Outline each blood parasite and name the species.
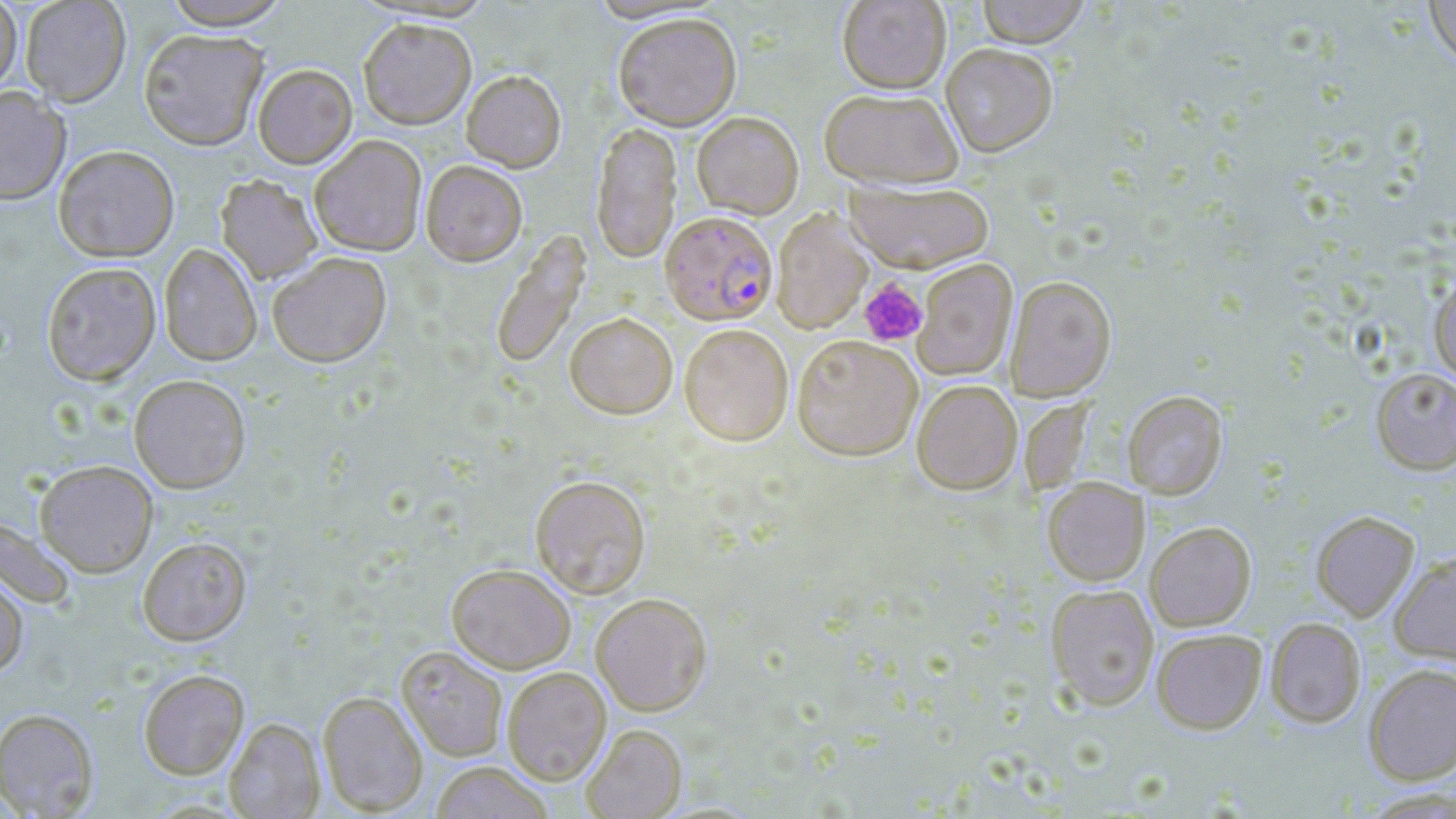
Approximate bounding boxes as (x1,y1)-(x2,y2) corner pairs in pixels.
Plasmodium falciparum-infected red blood cells: (660,211)-(777,325).
No Plasmodium ovale, Plasmodium malariae, Plasmodium vivax, Babesia divergens, or Trypanosoma brucei observed.

Uninfected red blood cell locations: (0,0)-(22,95), (20,0)-(131,106), (160,0)-(292,30), (837,0)-(951,93), (975,0)-(1092,47), (1424,0)-(1456,71), (612,12)-(742,131), (358,18)-(476,130), (138,28)-(269,149), (940,43)-(1058,157), (252,63)-(357,168), (461,69)-(566,172), (0,86)-(71,204), (818,87)-(963,189), (692,111)-(804,219), (591,121)-(682,264), (309,134)-(427,256), (54,145)-(179,261), (420,160)-(528,266), (216,175)-(323,283), (846,179)-(994,273), (772,209)-(872,334), (490,228)-(591,371), (159,243)-(262,366), (267,251)-(391,367), (913,258)-(1018,381), (41,262)-(161,385), (1429,273)-(1456,383), (1005,275)-(1117,400), (565,311)-(678,419), (679,324)-(793,445), (792,334)-(922,460), (1371,368)-(1456,474), (129,374)-(251,493), (911,379)-(1022,494), (1123,390)-(1228,499), (35,460)-(158,576), (530,475)-(651,598), (1043,478)-(1149,585), (1311,510)-(1420,621), (0,515)-(77,608), (1146,522)-(1256,630), (137,536)-(252,645), (1389,551)-(1456,664), (447,563)-(575,674), (0,570)-(29,678), (1046,584)-(1159,710), (591,593)-(712,715), (1266,617)-(1367,728), (1152,628)-(1267,733), (397,645)-(509,761), (1364,663)-(1456,784), (502,667)-(612,785), (138,669)-(249,779), (317,690)-(429,816), (0,708)-(99,818), (224,718)-(324,819), (581,724)-(687,819), (430,762)-(553,819). Platelet locations: (859,278)-(928,347). Slide-level diagnosis: Plasmodium falciparum. Captured at 1000x magnification. Thin blood film. Single field of view. May-Grünwald-Giemsa stain. Image is 1456×819 pixels. Light microscopy.